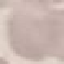
Result: negative for malaria parasites. Photographed with a smartphone camera at the microscope eyepiece. Giemsa-stained preparation. Thin blood film. Cell patch, automatically extracted from a larger field of view and resized to 64 × 64 pixels.